Assess this cell for malaria.
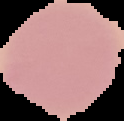
It is uninfected.

From a thin blood film. Image is 124×121 pixels. The area outside the segmented cell region is set to black.